Identify the parasite.
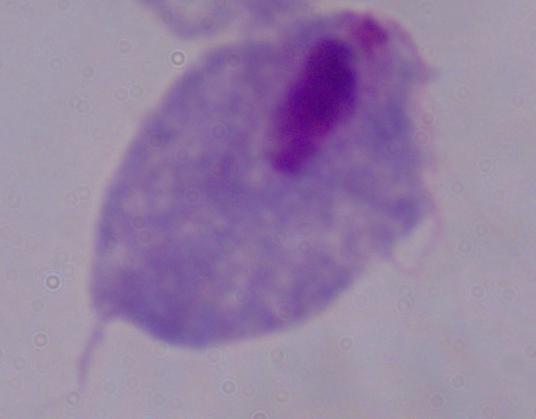

A trichomonad.

magnification = 1000x
modality = photomicrograph